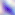

Summary:
  - Magnification: 400x
  - Identification: Toxoplasma gondii
  - Modality: photomicrograph